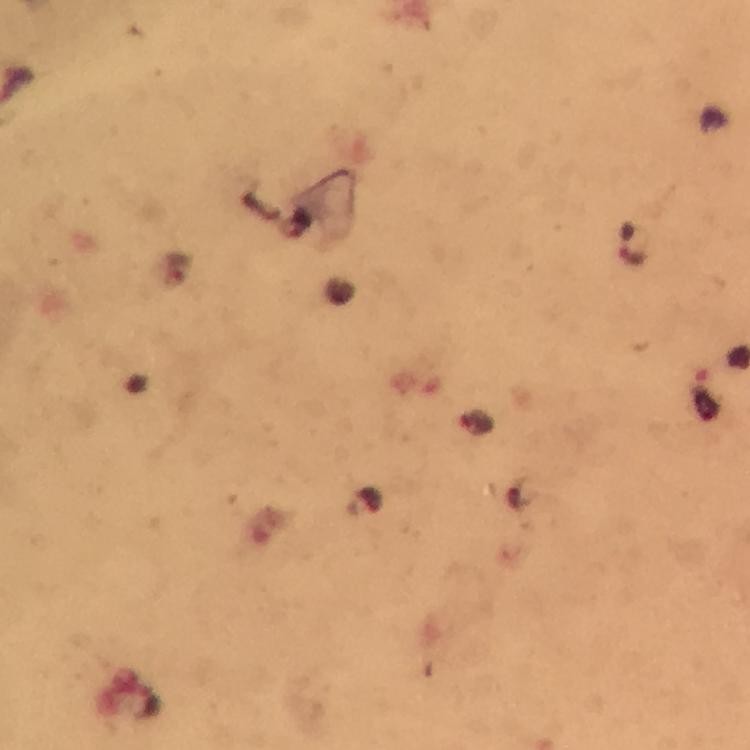
preparation = thick blood smear
image size = 750×750 pixels
capture = smartphone mounted on the microscope
malaria parasite locations = approximate object centers, in pixels from the top-left corner: (x=477, y=423)
immersion oil = applied
context = from a diagnostic examination for malaria
cropped from = a single field of view
stain = Giemsa
magnification = 100x